Name the parasite shown.
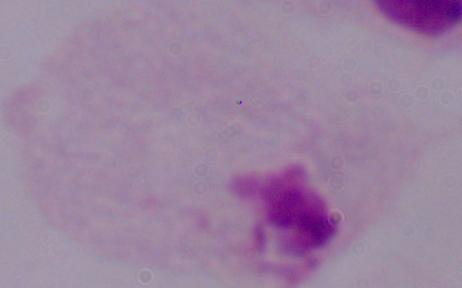
A trichomonad.

modality: micrograph
magnification: 1000x